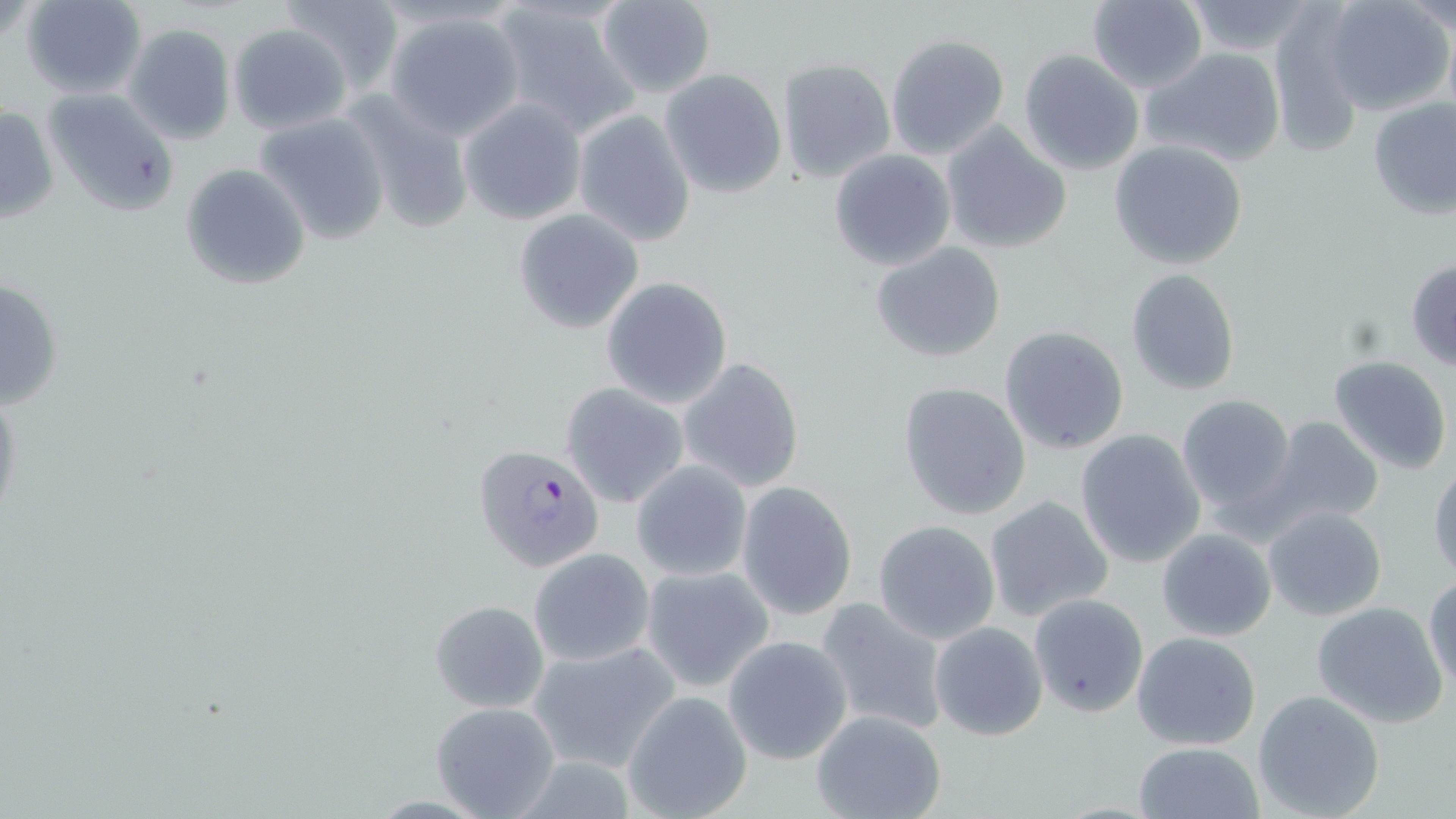

{
  "slide_level_diagnosis": "Plasmodium falciparum",
  "modality": "light microscopy",
  "preparation": "thin blood smear",
  "field_of_view": "single",
  "magnification": "1000x",
  "plasmodium_falciparum_infected_red_blood_cell_locations": "approximate bounding boxes as [x1, y1, x2, y2] in pixels: [473, 443, 606, 573]",
  "uninfected_red_blood_cell_locations": "approximate bounding boxes as [x1, y1, x2, y2] in pixels: [18, 0, 148, 98], [279, 0, 404, 92], [1086, 0, 1209, 92], [594, 1, 718, 100], [1182, 1, 1322, 55], [1322, 1, 1453, 115], [1396, 1, 1456, 37], [489, 2, 641, 136], [1267, 6, 1366, 158], [384, 8, 528, 139], [124, 22, 239, 145], [228, 23, 351, 134], [885, 33, 1010, 160], [78, 44, 221, 193], [1145, 48, 1287, 167], [1017, 50, 1143, 175], [777, 56, 895, 184], [659, 70, 787, 198], [42, 87, 181, 217], [344, 89, 476, 234], [458, 97, 587, 225], [1366, 98, 1456, 220], [0, 106, 60, 228], [253, 110, 392, 246], [573, 110, 697, 244], [940, 122, 1070, 255], [1109, 141, 1248, 269], [829, 149, 956, 271], [179, 162, 312, 291], [512, 210, 643, 334], [868, 241, 1009, 364], [1406, 259, 1456, 371], [1125, 269, 1241, 396], [601, 276, 732, 408], [0, 277, 64, 411], [999, 325, 1130, 453], [1329, 354, 1453, 474], [677, 356, 804, 493], [897, 381, 1032, 521], [0, 382, 24, 530], [559, 382, 691, 508], [1175, 394, 1297, 521], [1261, 417, 1384, 531], [1075, 430, 1206, 567], [629, 461, 753, 583], [1430, 462, 1456, 585], [735, 481, 858, 621], [983, 495, 1114, 623], [1262, 506, 1388, 622], [873, 520, 1000, 644], [1156, 528, 1277, 643], [528, 547, 655, 665], [639, 565, 774, 690], [1424, 574, 1456, 695], [1027, 593, 1148, 718], [814, 597, 948, 735], [426, 599, 551, 712], [1310, 601, 1449, 729], [930, 622, 1049, 739], [1131, 631, 1261, 750], [723, 636, 853, 765], [527, 641, 680, 772], [1251, 689, 1386, 818], [622, 691, 753, 819], [429, 701, 562, 818], [810, 709, 949, 819], [1132, 742, 1264, 819]",
  "stain": "May-Grünwald-Giemsa",
  "image_size": "1456×819 pixels"
}